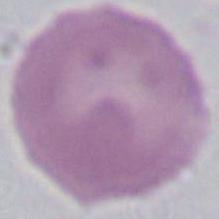

identification = red blood cell
magnification = 1000x
modality = photomicrograph